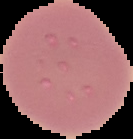
Summary:
  - Result: negative for Plasmodium parasites
  - Image size: 133×139 pixels
  - Image type: segmented cell region with the area outside set to black
  - Preparation: thin blood film